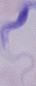

Summary:
  - Identification: trypanosome
  - Modality: micrograph
  - Magnification: 1000x